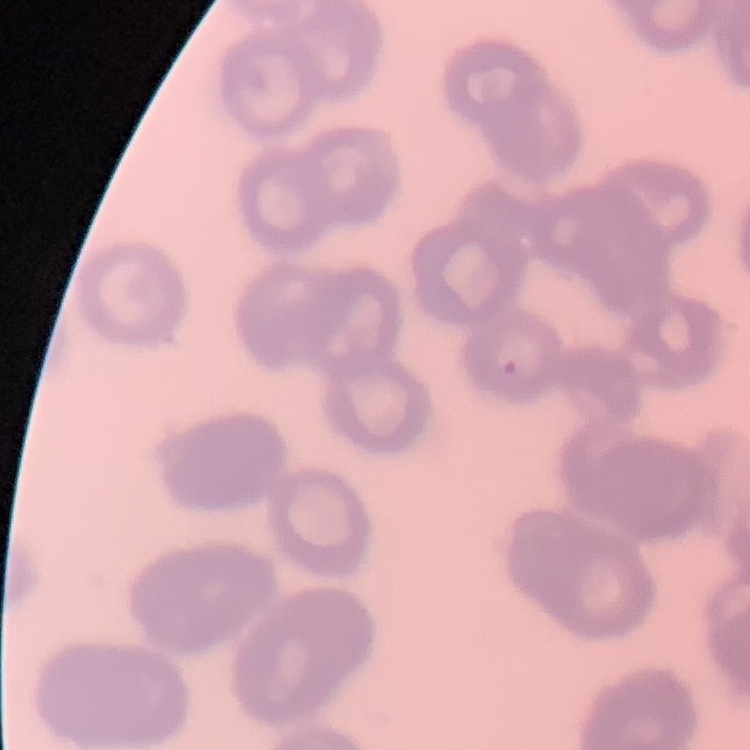
Summary:
  - Red blood cell morphology: rouleaux formation
  - Stain: Field's or Giemsa
  - Preparation: thin blood film
  - Image type: square crop of a larger photomicrograph